Comment on the morphology of the erythrocytes.
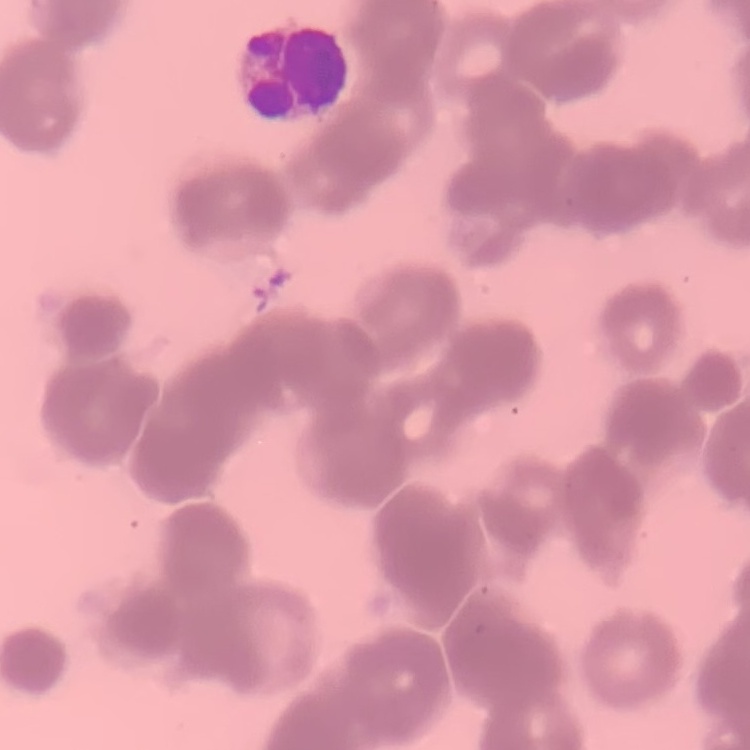
Rouleaux formation.

stain = Field's or Giemsa
preparation = thin blood smear
image type = square crop of a larger photomicrograph